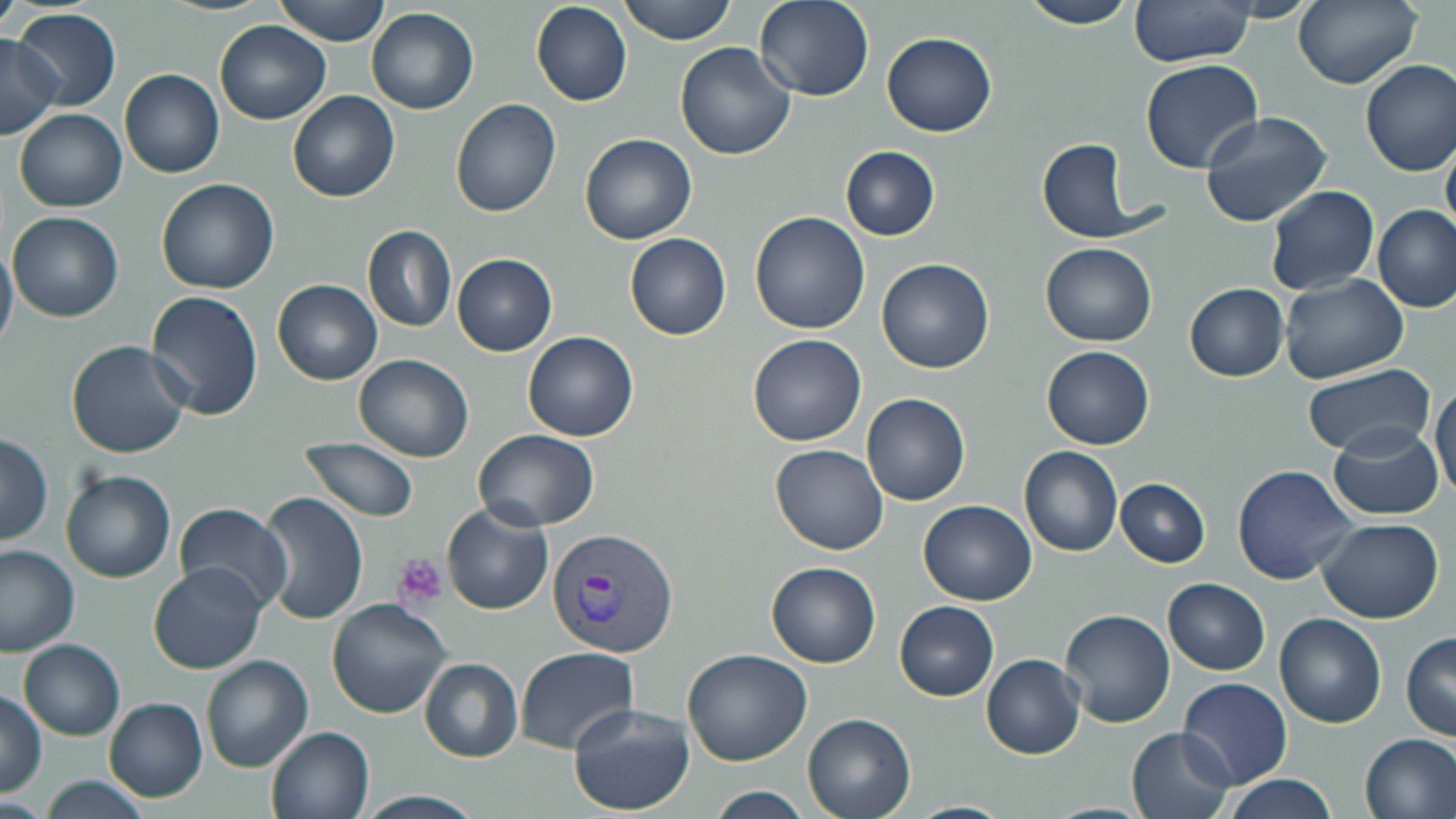
Summary:
  - Coordinate format: approximate bounding boxes as [x1, y1, x2, y2] in pixels
  - Uninfected red blood cell locations: [276, 0, 391, 46], [619, 0, 738, 45], [754, 0, 873, 102], [1018, 0, 1141, 28], [1294, 0, 1422, 89], [531, 2, 632, 106], [1129, 2, 1253, 67], [366, 7, 479, 114], [13, 8, 122, 110], [214, 20, 331, 124], [883, 32, 997, 137], [0, 35, 60, 140], [675, 42, 797, 161], [1359, 58, 1456, 176], [1140, 59, 1263, 173], [119, 69, 224, 179], [287, 90, 400, 202], [449, 99, 562, 219], [14, 108, 126, 212], [1200, 110, 1333, 227], [579, 133, 697, 245], [1441, 136, 1456, 246], [1037, 139, 1138, 239], [840, 146, 941, 240], [155, 178, 280, 294], [1263, 185, 1380, 296], [1374, 206, 1456, 312], [749, 211, 870, 334], [8, 212, 124, 322], [362, 225, 456, 332], [624, 233, 730, 340], [0, 239, 18, 357], [1040, 241, 1156, 346], [452, 254, 558, 357], [876, 258, 995, 374], [1279, 275, 1408, 386], [272, 279, 382, 385], [1184, 283, 1288, 381], [144, 290, 263, 422], [521, 332, 638, 441], [747, 333, 866, 447], [66, 340, 192, 459], [1042, 346, 1153, 449], [352, 354, 474, 461], [1301, 364, 1436, 456], [1430, 381, 1456, 504], [861, 393, 970, 507], [1329, 422, 1444, 520], [473, 430, 599, 529], [0, 434, 52, 546], [298, 437, 419, 523], [770, 444, 889, 555], [1019, 446, 1123, 557], [1233, 465, 1360, 584], [60, 469, 176, 583], [1116, 478, 1210, 567], [258, 492, 367, 623], [917, 499, 1037, 604], [173, 502, 293, 611], [442, 503, 552, 615], [1316, 518, 1444, 623], [0, 544, 79, 656], [149, 562, 267, 674], [766, 562, 882, 668], [1163, 579, 1271, 674], [326, 599, 452, 719], [894, 601, 998, 701], [1058, 609, 1176, 729], [1274, 612, 1387, 727], [1401, 632, 1456, 741], [18, 639, 125, 739], [515, 646, 638, 754], [683, 648, 812, 765], [982, 653, 1085, 759], [202, 654, 314, 773], [419, 657, 524, 762], [1177, 676, 1294, 789], [0, 690, 47, 797], [103, 697, 207, 802], [568, 702, 695, 817], [803, 713, 916, 819], [265, 724, 376, 818], [1127, 726, 1236, 819], [1357, 732, 1456, 819], [34, 774, 155, 819], [1225, 774, 1338, 819], [706, 787, 812, 819]
  - Platelet locations: [393, 553, 447, 606]
  - Plasmodium vivax-infected red blood cell locations: [547, 530, 679, 661]
  - Slide-level diagnosis: Plasmodium vivax
  - Stain: May-Grünwald-Giemsa
  - Field of view: one of a larger specimen
  - Image size: 1456×819 pixels
  - Magnification: 1000x
  - Modality: light microscopy
  - Preparation: thin blood film